Assess this cell for malaria.
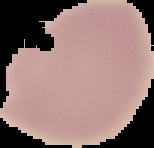
It is uninfected.

Summary:
  - Preparation: thin blood film
  - Image size: 154×148 pixels
  - Image type: cell region segmented out of the field of view; surrounding area masked to black